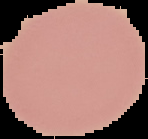
Malaria status: uninfected. The area outside the segmented cell region is set to black. From a thin blood smear. Image is 148×139 pixels.